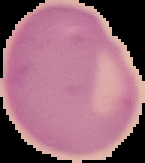

image_type: segmented cell region on a black background
image_size: 145×163 pixels
preparation: thin blood smear
malaria_status: uninfected